Assess this cell for malaria.
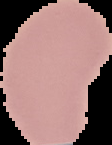
It is uninfected.

Summary:
  - Preparation: thin blood film
  - Image size: 112×145 pixels
  - Image type: cell region segmented out of the field of view; surrounding area masked to black